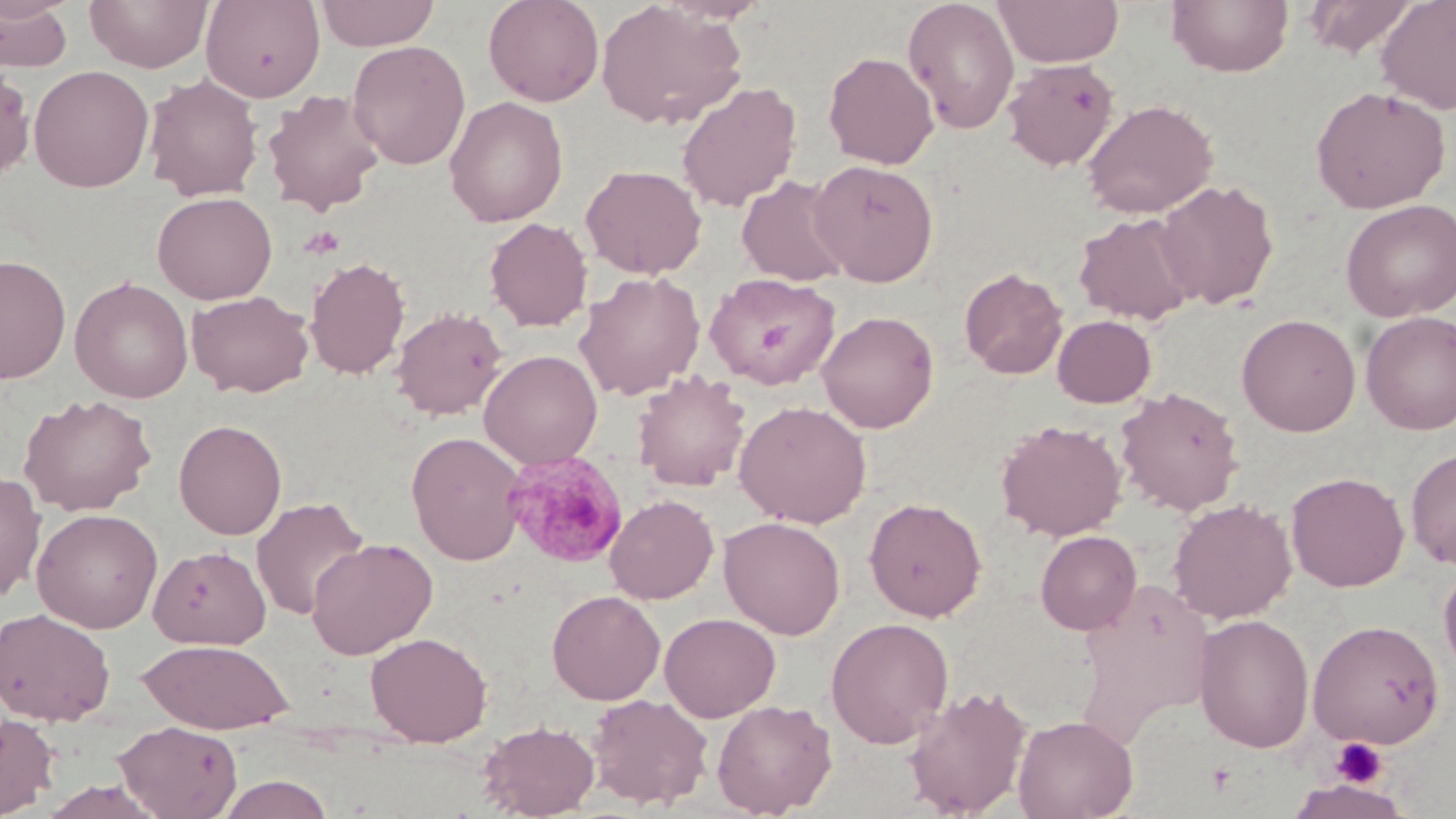
slide-level diagnosis = Plasmodium malariae
uninfected red blood cell locations = approximate bounding boxes as (x1,y1)-(x2,y2) corner pairs in pixels: (1,0)-(75,71), (84,0)-(213,72), (200,0)-(325,103), (315,0)-(440,50), (484,0)-(604,106), (902,0)-(1020,135), (993,0)-(1124,68), (1166,0)-(1293,77), (1302,0)-(1420,58), (1375,0)-(1456,114), (596,1)-(747,130), (347,40)-(470,169), (823,50)-(939,169), (1002,58)-(1119,171), (0,64)-(35,181), (28,64)-(154,193), (144,74)-(263,202), (676,81)-(802,213), (1310,86)-(1451,213), (262,89)-(386,216), (445,96)-(568,226), (1082,99)-(1218,218), (808,159)-(940,286), (580,164)-(707,279), (736,174)-(853,286), (1154,180)-(1279,310), (152,192)-(277,304), (1341,199)-(1456,322), (1073,212)-(1200,325), (484,217)-(593,332), (0,254)-(71,383), (304,257)-(410,380), (959,267)-(1068,379), (574,270)-(706,401), (704,272)-(841,389), (70,276)-(193,403), (186,290)-(313,398), (391,306)-(508,420), (817,310)-(939,433), (1361,311)-(1456,435), (1236,313)-(1361,436), (1052,314)-(1157,408), (478,350)-(603,469), (632,370)-(751,492), (1115,386)-(1244,515), (19,394)-(157,516), (733,400)-(872,528), (173,419)-(287,540), (995,419)-(1127,540), (407,431)-(527,566), (1406,446)-(1456,568), (0,470)-(47,601), (1286,471)-(1409,592), (604,494)-(718,604), (251,496)-(370,621), (864,497)-(987,622), (1168,498)-(1297,624), (31,508)-(163,634), (718,515)-(846,639), (1035,530)-(1141,635), (307,537)-(437,659), (148,545)-(271,649), (1438,559)-(1456,679), (547,590)-(665,705), (0,607)-(115,726), (659,612)-(781,721), (1193,614)-(1314,753), (826,618)-(954,747), (1307,619)-(1444,748), (365,632)-(492,746), (137,638)-(294,734), (902,685)-(1032,817), (586,693)-(713,810), (711,699)-(837,817), (0,713)-(60,818), (1013,714)-(1138,819), (477,719)-(600,818), (113,720)-(242,819), (214,773)-(336,818), (1287,778)-(1412,819), (37,779)-(168,819)
field of view = one of a larger specimen
magnification = 1000x
preparation = thin blood smear
Plasmodium malariae-infected red blood cell locations = approximate bounding boxes as (x1,y1)-(x2,y2) corner pairs in pixels: (503,451)-(628,568)
stain = May-Grünwald-Giemsa
platelet locations = approximate bounding boxes as (x1,y1)-(x2,y2) corner pairs in pixels: (1329,737)-(1388,789), (1206,762)-(1237,795)
modality = light microscopy
image size = 1456×819 pixels